Identify the parasite.
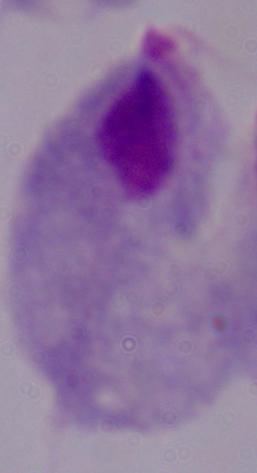

This is a trichomonad.

Summary:
  - Modality: micrograph
  - Magnification: 1000x